State which parasite is depicted.
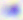
This is Toxoplasma gondii.

{
  "magnification": "400x",
  "modality": "photomicrograph"
}